Give the extent of all Plasmodium falciparum-infected red blood cells.
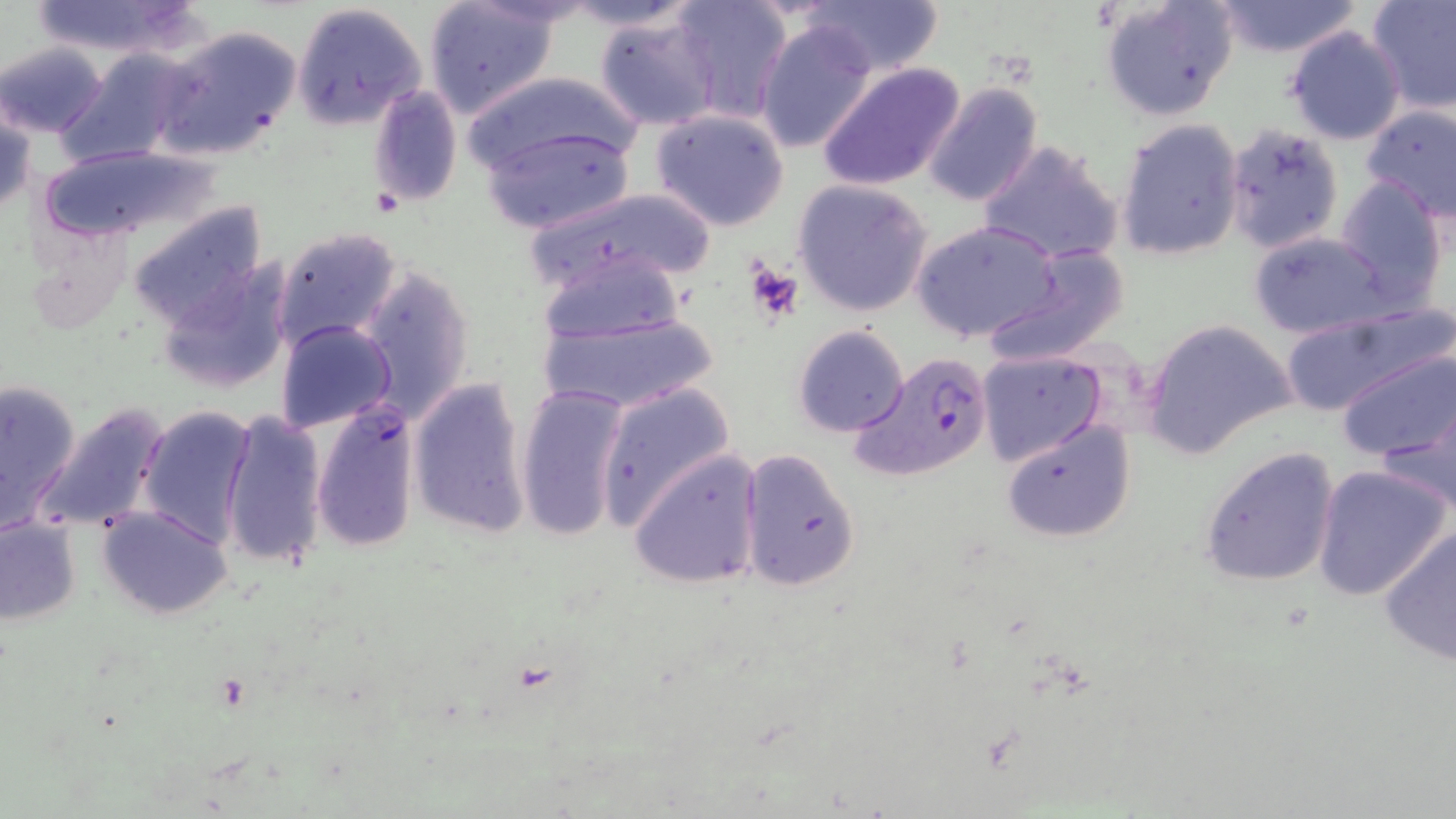
Approximate bounding boxes as (x1, y1, x2, y2) in pixels.
Plasmodium falciparum-infected red blood cells: (849, 350, 995, 484).

Platelet locations: (745, 258, 804, 324). Uninfected red blood cell locations: (27, 0, 200, 57), (556, 0, 701, 30), (669, 0, 794, 122), (795, 0, 946, 78), (1101, 0, 1237, 121), (1211, 0, 1362, 58), (1366, 0, 1456, 112), (424, 1, 561, 121), (289, 3, 427, 131), (593, 11, 723, 131), (755, 19, 879, 154), (154, 23, 302, 160), (1284, 26, 1407, 146), (1, 42, 108, 138), (57, 49, 189, 165), (816, 60, 966, 193), (459, 71, 644, 176), (921, 81, 1042, 208), (368, 83, 461, 209), (2, 101, 36, 218), (1360, 103, 1456, 224), (650, 108, 790, 231), (1115, 118, 1246, 261), (1224, 123, 1344, 255), (481, 125, 635, 234), (977, 140, 1126, 265), (36, 145, 212, 247), (1335, 175, 1449, 306), (792, 180, 933, 317), (520, 186, 716, 295), (124, 201, 269, 333), (910, 219, 1062, 343), (274, 226, 403, 351), (28, 227, 134, 335), (1249, 232, 1393, 338), (980, 246, 1131, 366), (535, 249, 688, 344), (159, 256, 294, 394), (356, 264, 475, 419), (1278, 302, 1449, 417), (532, 308, 723, 415), (1141, 318, 1296, 459), (277, 320, 397, 434), (792, 324, 908, 436), (1337, 348, 1453, 464), (975, 349, 1107, 468), (0, 375, 84, 526), (407, 377, 532, 537), (594, 381, 735, 526), (514, 383, 630, 542), (1376, 393, 1456, 520), (310, 395, 423, 555), (33, 404, 169, 534), (138, 405, 257, 546), (222, 411, 329, 571), (1000, 417, 1137, 543), (1198, 446, 1340, 587), (627, 448, 762, 590), (738, 449, 861, 591), (1311, 464, 1452, 602), (98, 505, 232, 619), (0, 516, 82, 625), (1378, 523, 1456, 666). Slide-level diagnosis: Plasmodium falciparum. Thin blood smear. One field of a larger specimen. Light microscopy. May-Grünwald-Giemsa-stained preparation. Image is 1456×819 pixels. 1000x magnification.